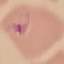

Summary:
  - Malaria status: parasitized
  - Stain: Giemsa
  - Preparation: thin smear
  - Image type: automatically extracted cell patch, resized to 64 × 64 pixels
  - Capture: smartphone camera at the microscope eyepiece